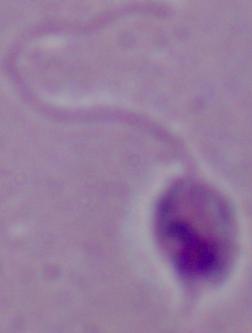 Captured at 1000x magnification. Micrograph. A Leishmania parasite is seen.